Locate every blood parasite and identify its species.
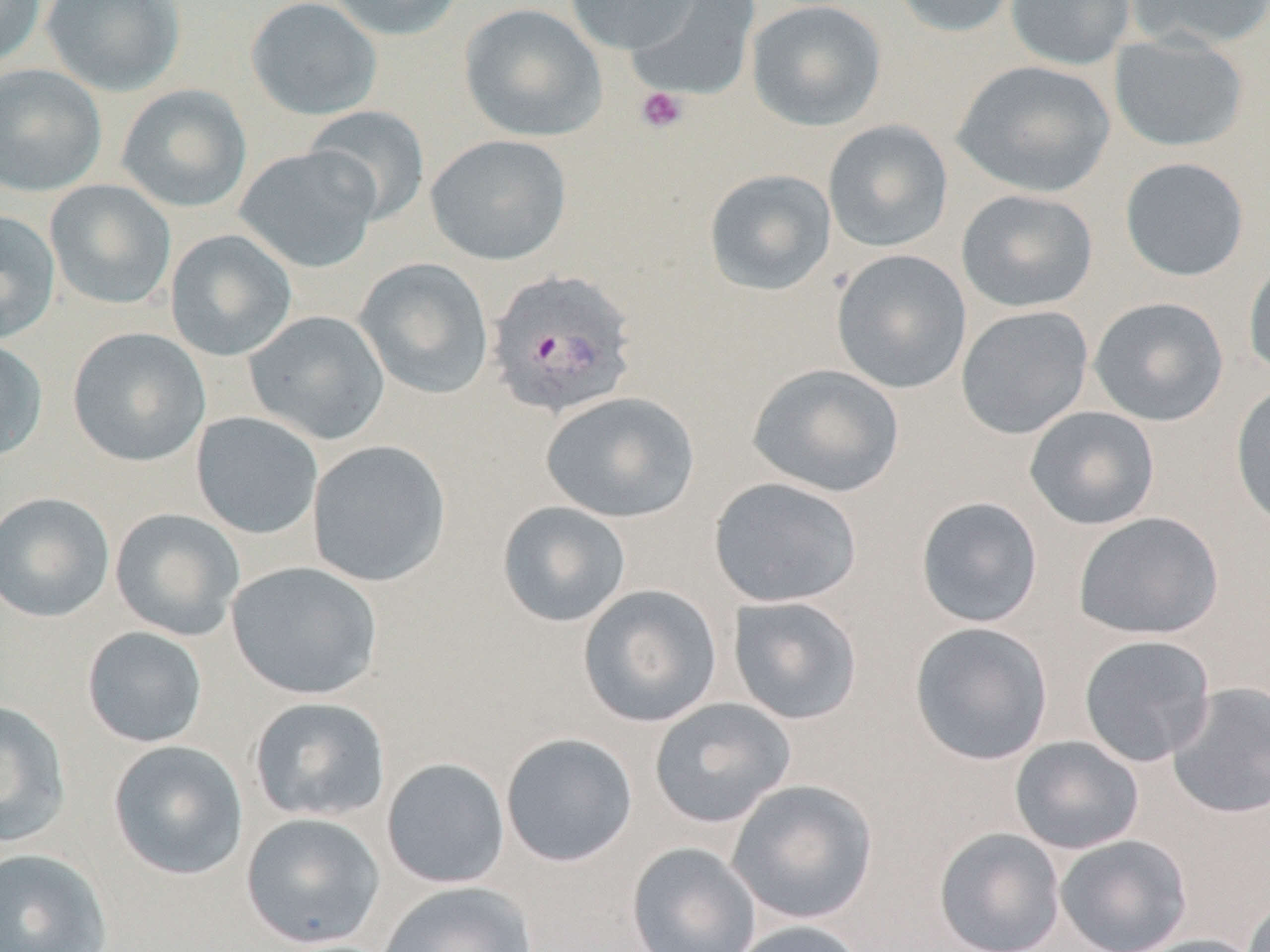
Approximate bounding boxes as (x1,y1)-(x2,y2) corner pairs in pixels.
Plasmodium vivax-infected red blood cells: (486,269)-(639,420).
No Plasmodium falciparum, Plasmodium ovale, Plasmodium malariae, Babesia divergens, or Trypanosoma brucei observed.

Summary:
  - Uninfected red blood cell locations: (0,0)-(45,67), (40,0)-(186,97), (246,0)-(382,121), (325,0)-(466,42), (564,0)-(699,54), (624,0)-(762,102), (890,0)-(1021,38), (1004,0)-(1136,71), (1125,0)-(1270,51), (746,1)-(887,131), (459,3)-(607,142), (1108,32)-(1250,153), (951,60)-(1117,198), (0,63)-(107,198), (116,84)-(252,213), (304,105)-(431,227), (823,120)-(954,252), (425,134)-(572,265), (234,145)-(380,273), (1119,157)-(1250,281), (703,168)-(837,296), (44,179)-(177,310), (955,189)-(1099,313), (0,210)-(61,344), (165,228)-(297,361), (830,249)-(972,394), (1243,256)-(1270,379), (354,257)-(494,400), (1088,296)-(1229,426), (955,305)-(1094,439), (244,310)-(390,445), (67,327)-(211,467), (0,338)-(48,462), (747,363)-(906,498), (1230,381)-(1270,531), (541,391)-(700,523), (1023,406)-(1160,530), (191,411)-(323,540), (307,439)-(452,587), (708,476)-(863,608), (0,491)-(115,623), (915,496)-(1044,628), (496,501)-(632,628), (110,508)-(245,641), (1072,512)-(1224,640), (226,561)-(383,700), (577,584)-(723,728), (727,595)-(864,725), (909,621)-(1053,766), (82,626)-(208,748), (1078,635)-(1216,767), (1166,681)-(1270,819), (248,696)-(391,823), (649,697)-(797,828), (0,699)-(71,848), (500,732)-(638,867), (1009,735)-(1145,854), (108,739)-(249,881), (380,757)-(511,889), (726,779)-(878,924), (240,811)-(386,949), (933,827)-(1066,952), (1054,834)-(1192,952), (626,842)-(762,952), (0,847)-(114,952), (376,881)-(538,952), (1242,893)-(1270,952), (728,919)-(868,952), (1130,934)-(1266,952)
  - Platelet locations: (635,86)-(688,134)
  - Slide-level diagnosis: Plasmodium vivax
  - Magnification: 1000x
  - Modality: optical microscopy
  - Stain: May-Grünwald-Giemsa
  - Preparation: thin blood film
  - Field of view: single
  - Image size: 1270×952 pixels